Assess the morphology of the erythrocytes.
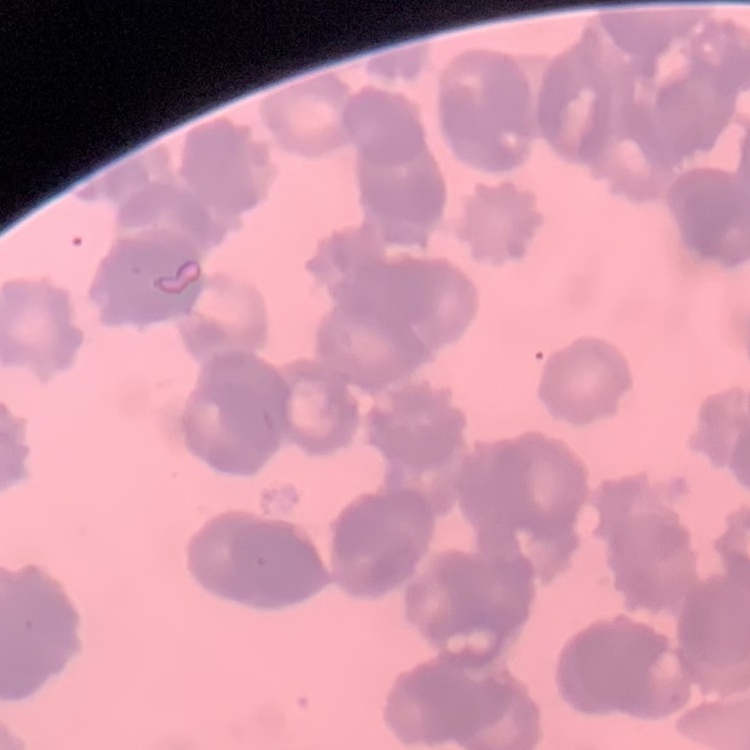
Rouleaux formation.

Thin peripheral smear. Field's or Giemsa stain. Square crop of a larger photomicrograph.